Describe the morphology of the red blood cells.
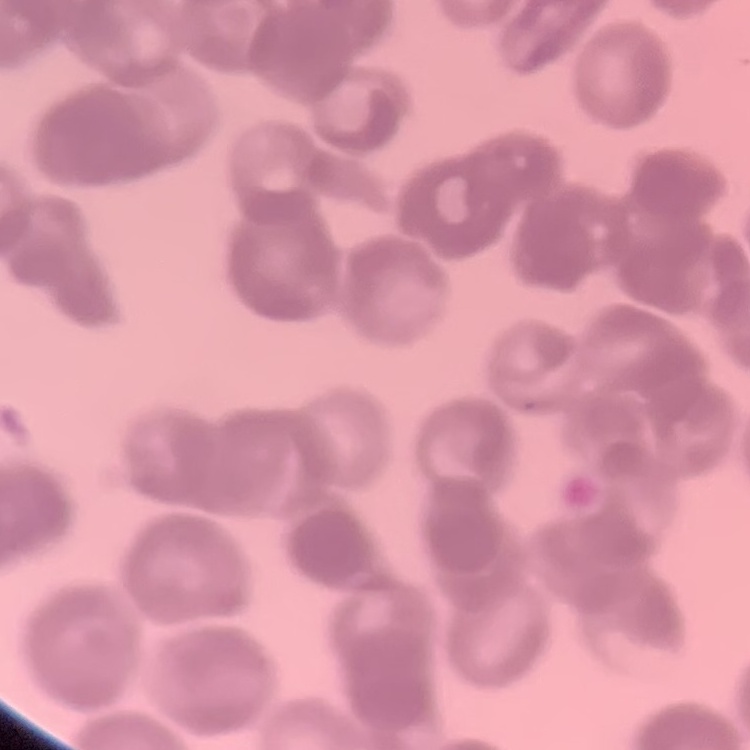
They show rouleaux formation.

stain = Field's or Giemsa
image type = square crop of a larger photomicrograph
preparation = thin peripheral smear